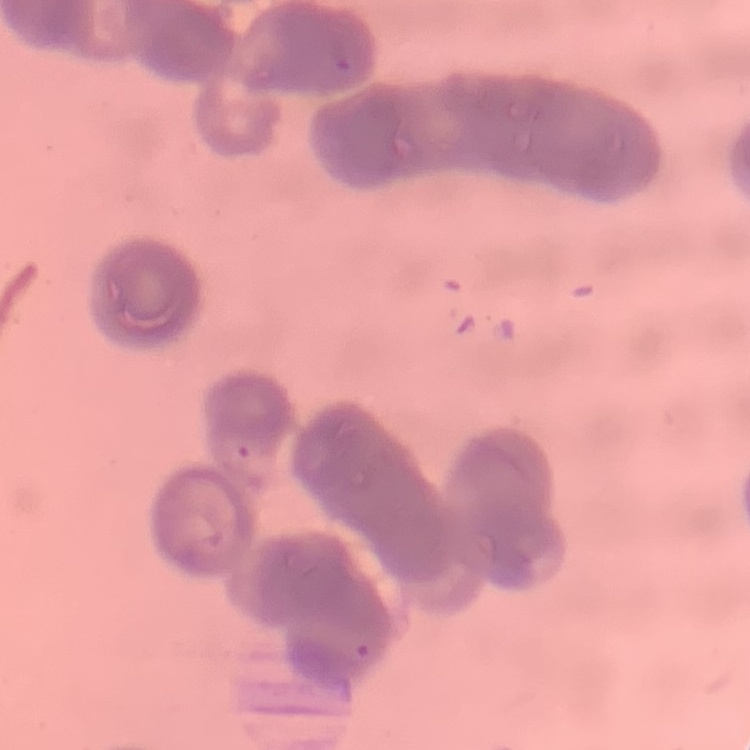

Summary:
  - Red blood cell morphology: rouleaux formation
  - Stain: Field's or Giemsa
  - Image type: square crop of a larger photomicrograph
  - Preparation: thin blood film